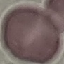 Malaria status: uninfected. Thin blood smear. Acquired by smartphone through the microscope eyepiece. Cell patch, automatically extracted from a larger field of view and resized to 64 × 64 pixels. Giemsa-stained preparation.